Classify this cell by malaria status.
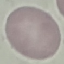
Uninfected.

Summary:
  - Image type: automatically extracted cell patch, resized to 64 × 64 pixels
  - Preparation: thin smear
  - Capture: smartphone through the microscope eyepiece
  - Stain: Giemsa